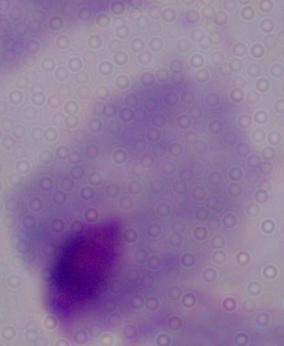
Captured at 1000x magnification. Micrograph. A trichomonad is seen.